Evaluate for malaria.
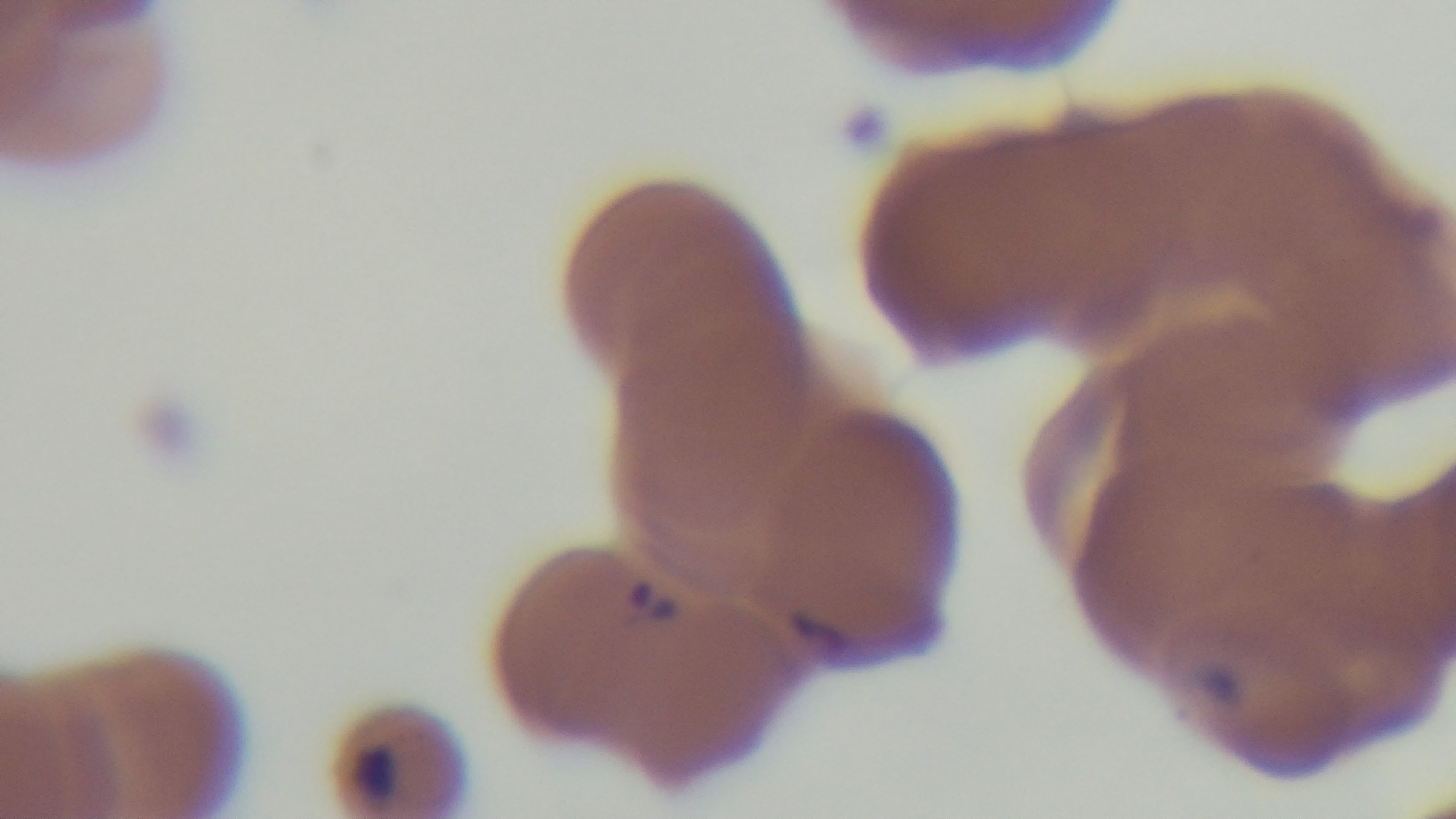

Positive.

field of view = single
objective = 100x oil immersion
stain = Giemsa
capture = mounted 4K digital camera
preparation = thin
modality = light microscopy